Comment on the morphology of the red blood cells.
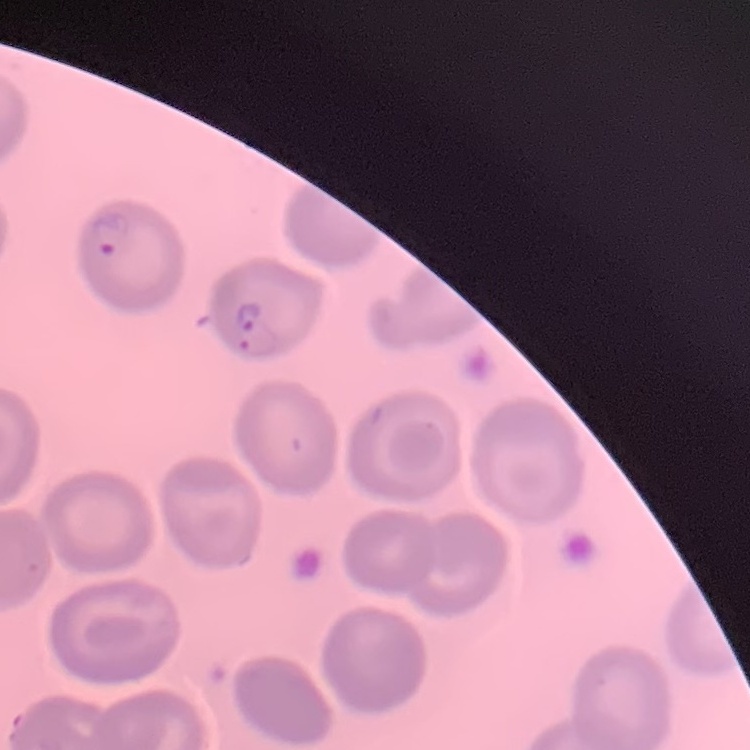
No rouleaux formation.

{
  "stain": "Field's or Giemsa",
  "preparation": "thin blood film",
  "image_type": "square crop of a larger photomicrograph"
}